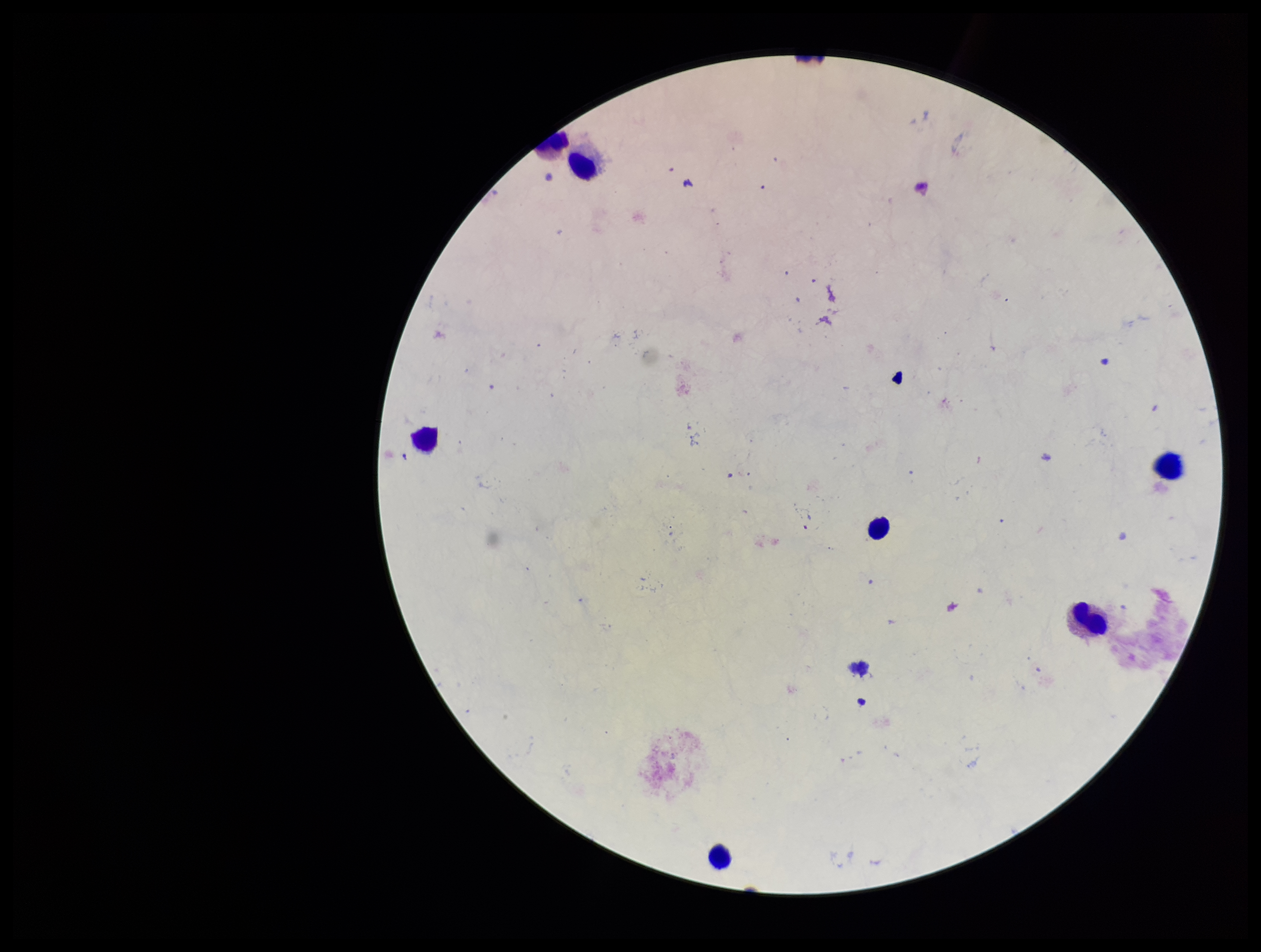
{
  "leukocyte_count": 7,
  "field_of_view": "single",
  "plasmodium_parasites": "none identified",
  "image_size": "1261×952 pixels",
  "stain": "Giemsa",
  "parasite_count": 0,
  "patient_malaria_status": "negative",
  "preparation": "thick smear",
  "capture": "smartphone photograph through the microscope eyepiece"
}